Mark where platelets are.
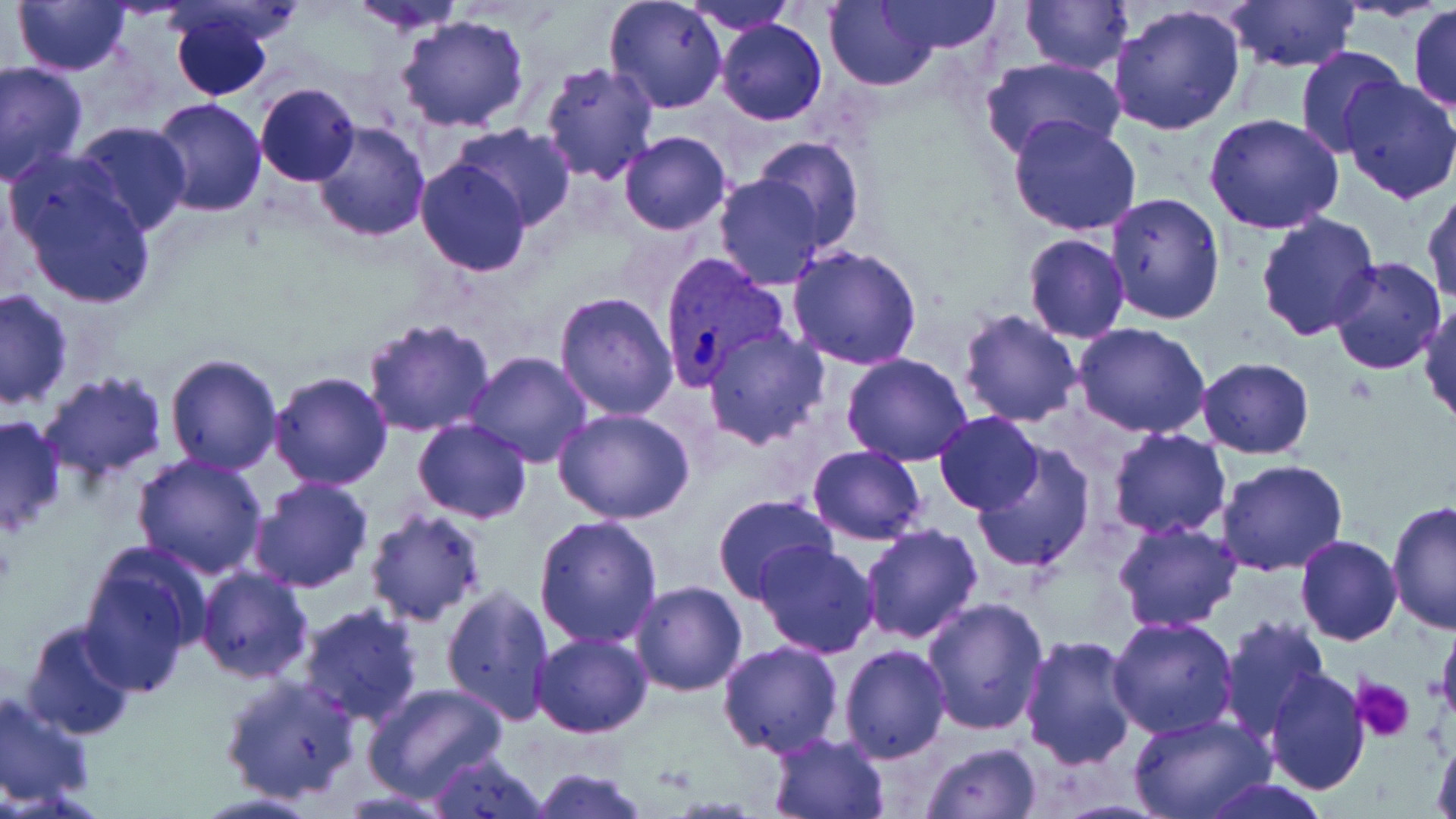
Approximate bounding boxes as (x1, y1, x2, y2) in pixels.
Platelets: (1352, 676, 1414, 742).

slide-level diagnosis = Plasmodium vivax
modality = optical microscopy
image size = 1456×819 pixels
Plasmodium vivax-infected red blood cell locations = approximate bounding boxes as (x1, y1, x2, y2) in pixels: (658, 254, 789, 390)
preparation = thin blood film
stain = May-Grünwald-Giemsa
uninfected red blood cell locations = approximate bounding boxes as (x1, y1, x2, y2) in pixels: (11, 0, 130, 75), (349, 0, 468, 32), (604, 0, 727, 114), (681, 0, 796, 35), (825, 0, 942, 90), (874, 0, 1005, 56), (1021, 0, 1133, 74), (1223, 2, 1361, 74), (1108, 4, 1246, 138), (1408, 4, 1456, 114), (169, 6, 276, 102), (395, 16, 530, 134), (714, 17, 829, 126), (1294, 45, 1405, 159), (980, 56, 1124, 164), (1, 60, 88, 185), (539, 62, 660, 183), (0, 77, 149, 212), (1338, 78, 1456, 203), (255, 82, 360, 185), (149, 98, 267, 218), (1203, 113, 1344, 234), (1007, 114, 1143, 238), (70, 122, 191, 235), (312, 122, 432, 242), (452, 123, 576, 229), (618, 131, 732, 236), (753, 137, 866, 251), (5, 157, 158, 311), (415, 157, 532, 276), (713, 173, 827, 289), (1422, 185, 1456, 304), (1104, 191, 1226, 325), (1255, 212, 1383, 340), (1024, 233, 1130, 342), (787, 244, 923, 368), (981, 247, 1116, 405), (1329, 256, 1446, 376), (1, 286, 75, 411), (552, 291, 678, 421), (1418, 300, 1455, 426), (958, 308, 1085, 427), (486, 312, 671, 451), (360, 317, 496, 440), (1074, 323, 1209, 439), (702, 326, 830, 450), (464, 351, 592, 468), (841, 353, 972, 466), (164, 354, 283, 475), (1196, 358, 1315, 459), (36, 372, 169, 482), (269, 372, 392, 491), (554, 408, 697, 526), (934, 411, 1043, 513), (0, 413, 66, 536), (410, 419, 533, 523), (1107, 427, 1232, 539), (970, 442, 1095, 570), (807, 444, 927, 545), (131, 453, 268, 580), (1217, 458, 1349, 575), (249, 476, 374, 594), (712, 494, 838, 605), (1387, 498, 1456, 635), (363, 508, 490, 628), (533, 514, 663, 649), (1114, 521, 1242, 634), (858, 522, 983, 645), (1294, 534, 1403, 645), (755, 542, 880, 659), (76, 550, 203, 696), (194, 566, 314, 683), (629, 581, 746, 696), (440, 583, 556, 727), (921, 597, 1048, 737), (295, 603, 424, 728), (1108, 615, 1239, 739), (1216, 615, 1329, 742), (1435, 617, 1456, 736), (21, 619, 136, 739), (532, 633, 652, 738), (1019, 635, 1141, 771), (718, 641, 843, 757), (837, 644, 951, 764), (1265, 668, 1369, 795), (218, 672, 364, 805), (361, 681, 508, 803), (0, 689, 95, 811), (1128, 714, 1273, 819), (1429, 732, 1455, 819), (766, 733, 891, 819), (921, 741, 1040, 819), (425, 748, 548, 818), (531, 768, 649, 819), (1198, 777, 1328, 818)
magnification = 1000x
field of view = single